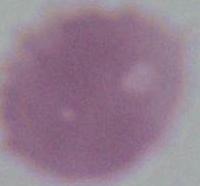 A red blood cell is shown. Photomicrograph. 1000x magnification.